Identify the parasite.
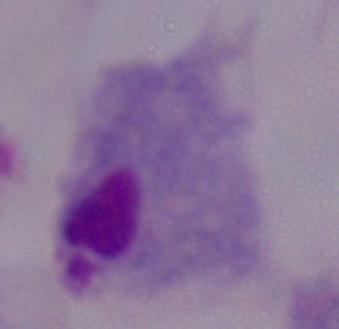

A trichomonad.

Micrograph. Captured at 1000x magnification.